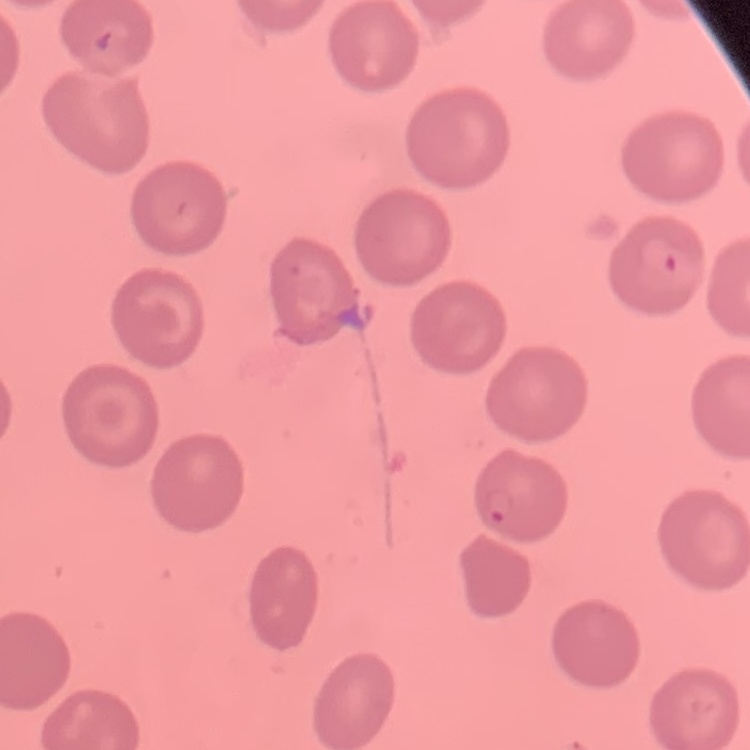
red blood cell morphology = no rouleaux formation
stain = Field's or Giemsa
image type = one tile cut from a larger photomicrograph
preparation = thin peripheral smear